Report the malaria status of this cell.
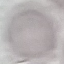

It is uninfected.

stain: Giemsa
preparation: thin blood smear
image_type: cell patch, automatically extracted from a larger field of view and resized to 64 × 64 pixels
capture: smartphone camera at the microscope eyepiece